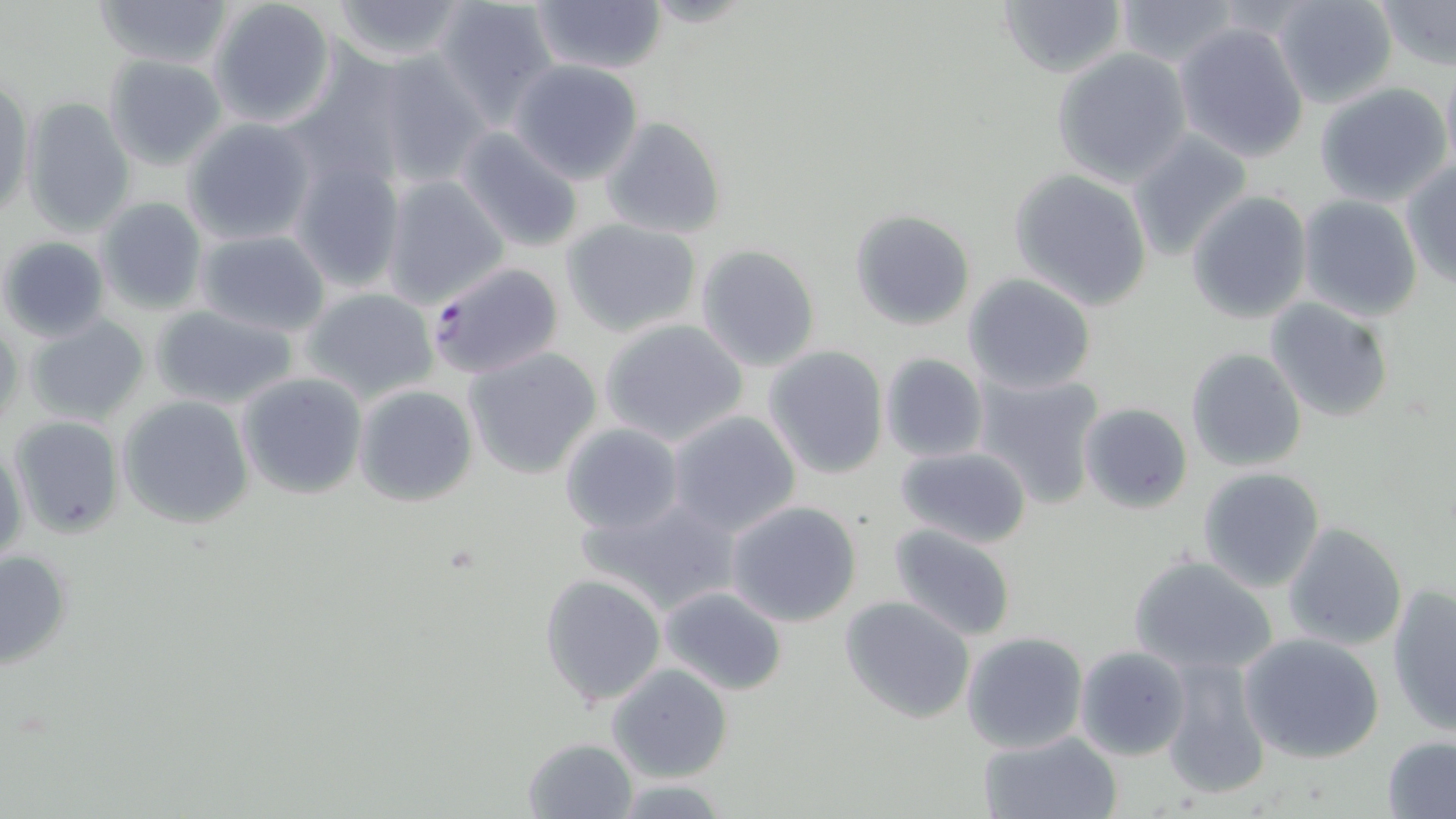

Summary:
  - Coordinate format: approximate bounding boxes as named x1/y1/x2/y2 corners in pixels
  - Plasmodium falciparum-infected red blood cell locations: (x1=426, y1=260, x2=565, y2=378)
  - Uninfected red blood cell locations: (x1=95, y1=0, x2=233, y2=70), (x1=328, y1=0, x2=470, y2=65), (x1=998, y1=0, x2=1127, y2=77), (x1=1114, y1=0, x2=1244, y2=66), (x1=1272, y1=0, x2=1398, y2=107), (x1=1376, y1=0, x2=1456, y2=70), (x1=208, y1=1, x2=338, y2=129), (x1=432, y1=1, x2=560, y2=123), (x1=531, y1=1, x2=666, y2=77), (x1=1175, y1=21, x2=1310, y2=163), (x1=1052, y1=48, x2=1193, y2=187), (x1=368, y1=51, x2=490, y2=189), (x1=103, y1=53, x2=229, y2=171), (x1=509, y1=60, x2=644, y2=184), (x1=1441, y1=61, x2=1456, y2=177), (x1=1, y1=79, x2=34, y2=221), (x1=1315, y1=82, x2=1454, y2=208), (x1=21, y1=97, x2=136, y2=237), (x1=181, y1=117, x2=316, y2=246), (x1=602, y1=117, x2=727, y2=238), (x1=453, y1=126, x2=586, y2=254), (x1=1127, y1=131, x2=1252, y2=261), (x1=291, y1=159, x2=407, y2=292), (x1=1400, y1=160, x2=1456, y2=288), (x1=1009, y1=170, x2=1152, y2=309), (x1=380, y1=173, x2=509, y2=309), (x1=1187, y1=191, x2=1312, y2=324), (x1=1297, y1=195, x2=1423, y2=320), (x1=96, y1=196, x2=207, y2=315), (x1=849, y1=209, x2=976, y2=330), (x1=562, y1=219, x2=702, y2=338), (x1=196, y1=229, x2=331, y2=336), (x1=1, y1=235, x2=111, y2=344), (x1=695, y1=245, x2=821, y2=371), (x1=962, y1=273, x2=1098, y2=394), (x1=301, y1=288, x2=441, y2=404), (x1=1265, y1=298, x2=1393, y2=424), (x1=151, y1=303, x2=299, y2=410), (x1=25, y1=314, x2=152, y2=427), (x1=600, y1=318, x2=749, y2=446), (x1=0, y1=321, x2=23, y2=432), (x1=763, y1=345, x2=890, y2=479), (x1=464, y1=347, x2=603, y2=479), (x1=1186, y1=347, x2=1307, y2=470), (x1=880, y1=353, x2=988, y2=461), (x1=353, y1=365, x2=598, y2=492), (x1=236, y1=371, x2=367, y2=499), (x1=975, y1=372, x2=1104, y2=508), (x1=352, y1=384, x2=478, y2=506), (x1=118, y1=396, x2=256, y2=527), (x1=1079, y1=402, x2=1193, y2=515), (x1=667, y1=409, x2=801, y2=536), (x1=7, y1=414, x2=125, y2=539), (x1=559, y1=422, x2=685, y2=535), (x1=0, y1=440, x2=28, y2=568), (x1=895, y1=445, x2=1032, y2=547), (x1=1198, y1=466, x2=1326, y2=592), (x1=580, y1=495, x2=743, y2=616), (x1=726, y1=501, x2=862, y2=627), (x1=1281, y1=522, x2=1408, y2=652), (x1=887, y1=524, x2=1020, y2=642), (x1=0, y1=549, x2=73, y2=672), (x1=1128, y1=553, x2=1279, y2=676), (x1=539, y1=572, x2=667, y2=708), (x1=1387, y1=584, x2=1456, y2=736), (x1=657, y1=585, x2=788, y2=696), (x1=840, y1=595, x2=976, y2=724), (x1=960, y1=631, x2=1090, y2=754), (x1=1238, y1=632, x2=1385, y2=763), (x1=1076, y1=646, x2=1192, y2=761), (x1=1160, y1=654, x2=1271, y2=800), (x1=608, y1=663, x2=732, y2=782), (x1=977, y1=730, x2=1121, y2=819), (x1=522, y1=736, x2=638, y2=818), (x1=1381, y1=737, x2=1456, y2=818), (x1=609, y1=779, x2=736, y2=816)
  - Slide-level diagnosis: Plasmodium falciparum
  - Field of view: single
  - Preparation: thin blood film
  - Magnification: 1000x
  - Stain: May-Grünwald-Giemsa
  - Image size: 1456×819 pixels
  - Modality: optical microscopy